Assess the morphology of the erythrocytes.
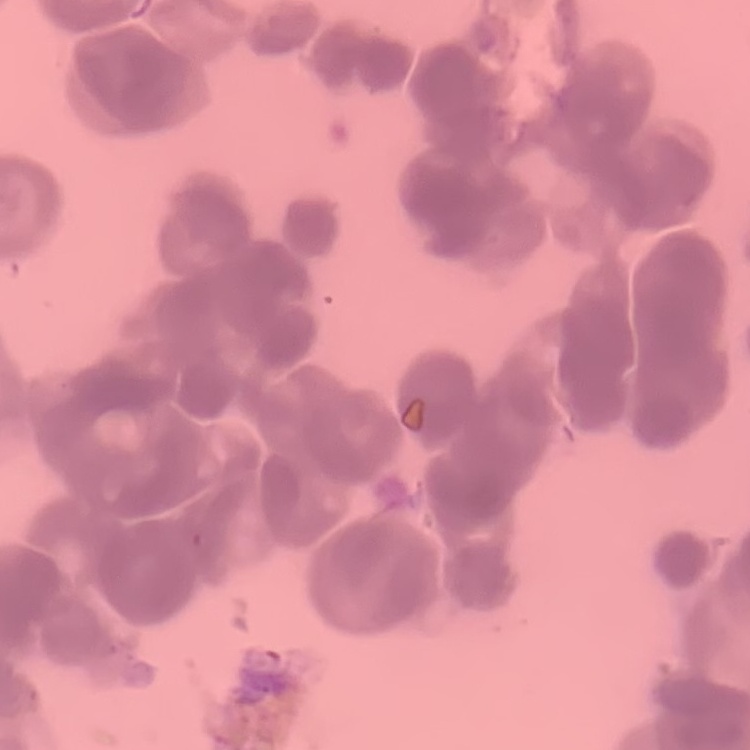
They show rouleaux formation.

Field's or Giemsa stain. Thin blood smear. Square crop of a larger photomicrograph.